Assess for Plasmodium parasites.
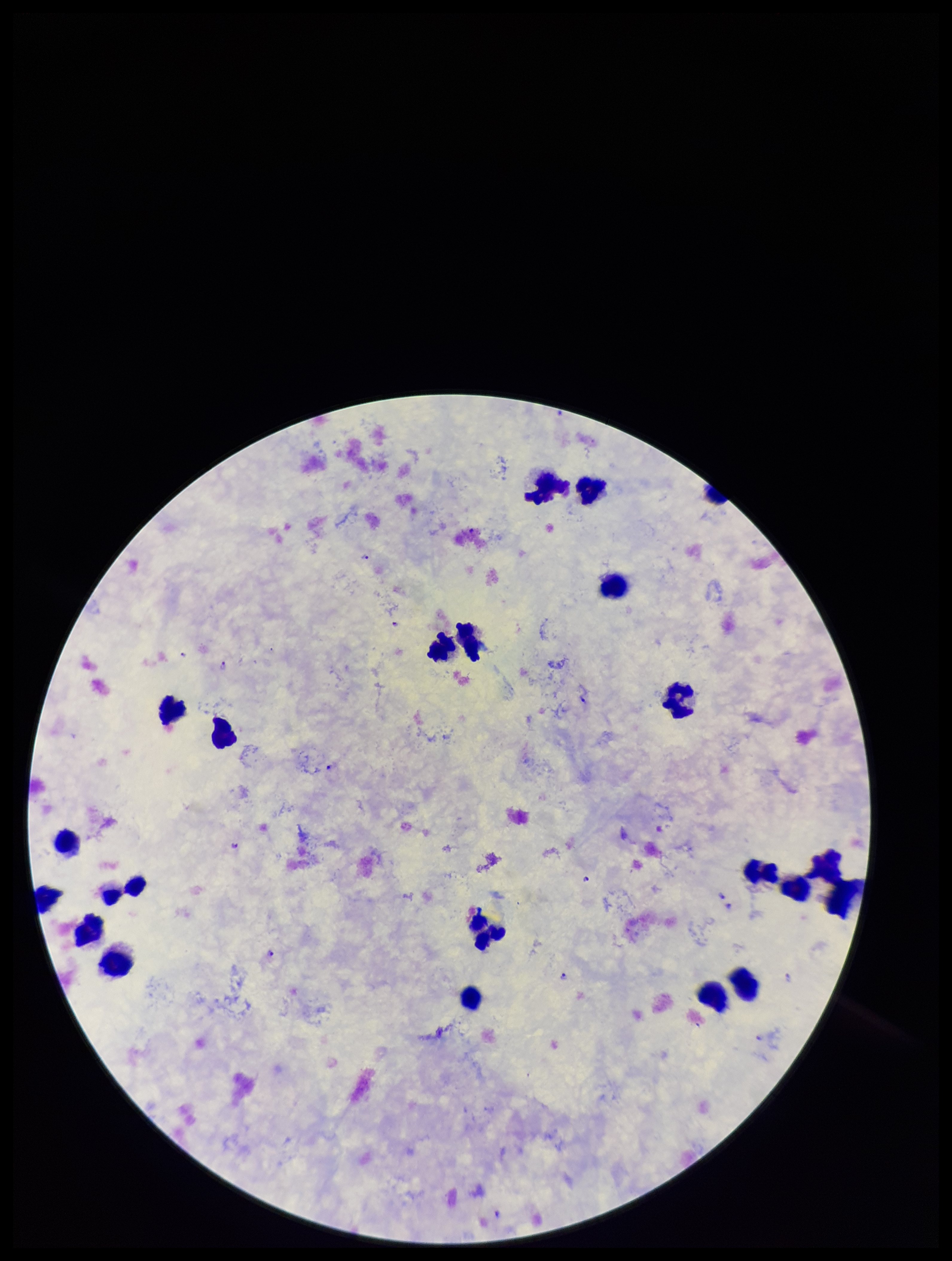

Seen.

Leukocyte count: 22. Preparation: thick blood smear. Stained with Giemsa. Smartphone photograph taken through the eyepiece of a microscope. Parasite count: 10. Patient malaria status: infected. Image is 952×1261 pixels. Species reported for this patient: Plasmodium falciparum. Single field of view.